Locate and identify every blood parasite.
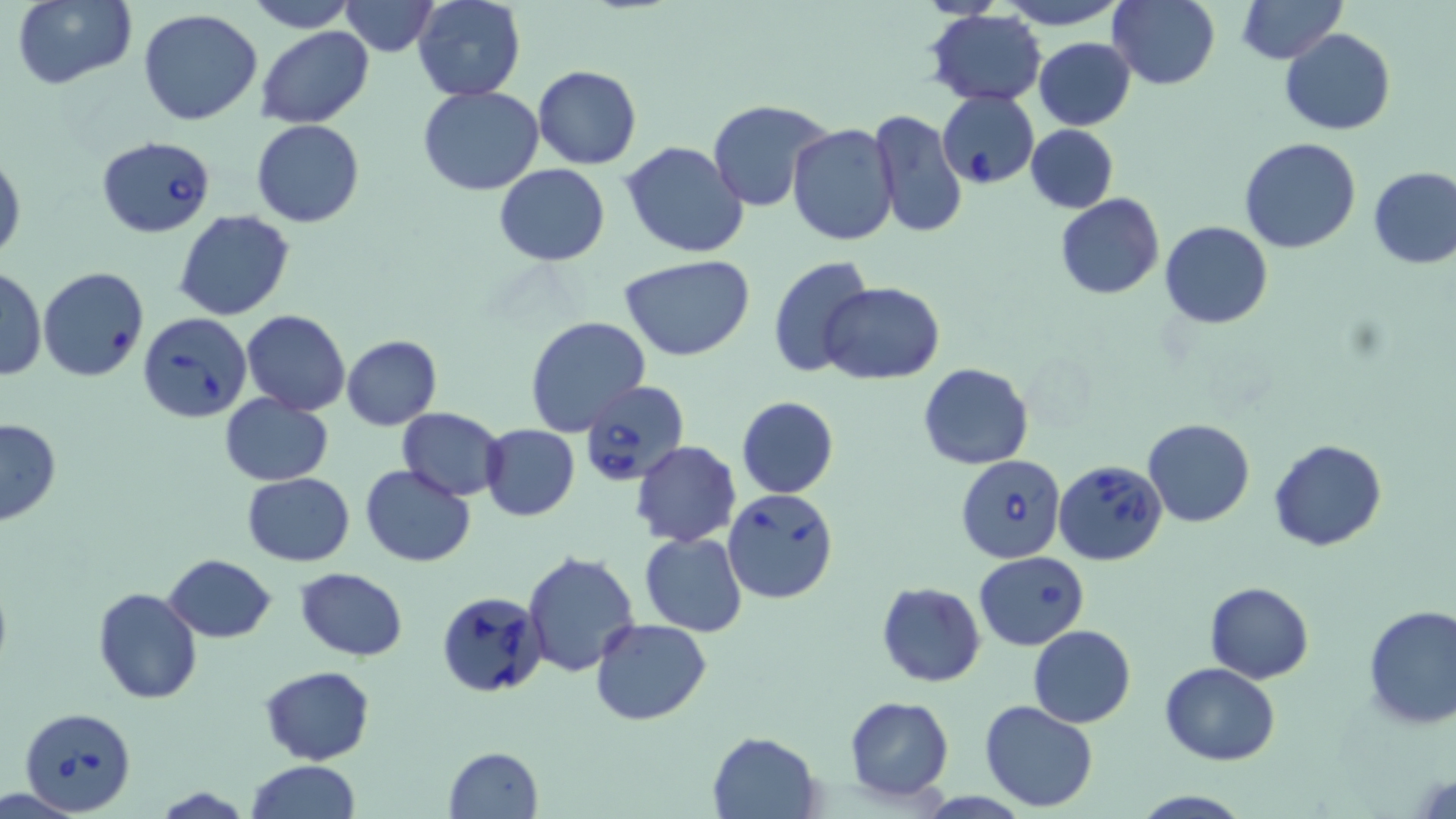
Approximate bounding boxes as (x1,y1)-(x2,y2) corner pairs in pixels.
Babesia divergens-infected red blood cells: (937,90)-(1039,189), (97,135)-(217,237), (136,311)-(252,422), (579,382)-(690,485), (955,454)-(1065,563), (1054,459)-(1168,566), (722,487)-(841,605), (436,590)-(548,699), (19,706)-(137,814).
No Plasmodium falciparum, Plasmodium ovale, Plasmodium malariae, Plasmodium vivax, or Trypanosoma brucei observed.

slide-level diagnosis = Babesia divergens
stain = May-Grünwald-Giemsa
image size = 1456×819 pixels
preparation = thin blood smear
uninfected red blood cell locations = approximate bounding boxes as (x1,y1)-(x2,y2) corner pairs in pixels: (9,0)-(141,91), (242,0)-(357,32), (412,0)-(526,102), (997,0)-(1129,29), (1108,0)-(1219,89), (1236,0)-(1344,64), (337,2)-(437,55), (924,8)-(1050,108), (138,9)-(265,127), (256,27)-(373,127), (1281,28)-(1396,135), (1033,37)-(1136,130), (533,65)-(641,168), (419,87)-(545,196), (708,99)-(837,213), (867,109)-(967,244), (251,119)-(365,229), (787,124)-(900,246), (1026,125)-(1119,212), (1241,139)-(1362,255), (620,140)-(748,258), (0,149)-(24,264), (495,164)-(609,266), (1369,166)-(1456,269), (1055,193)-(1165,300), (175,210)-(295,320), (1160,220)-(1273,329), (620,254)-(755,361), (767,255)-(877,381), (0,267)-(46,381), (38,267)-(150,382), (820,282)-(945,383), (242,309)-(351,415), (523,315)-(651,435), (340,334)-(442,431), (917,363)-(1034,470), (219,392)-(334,486), (736,396)-(839,498), (396,407)-(508,500), (0,417)-(60,525), (1142,419)-(1254,527), (480,424)-(580,521), (1268,439)-(1388,551), (631,441)-(741,547), (359,463)-(478,566), (242,471)-(355,566), (640,532)-(747,637), (521,549)-(642,679), (974,551)-(1090,650), (164,554)-(276,642), (295,566)-(407,662), (877,581)-(985,687), (1204,582)-(1313,683), (92,586)-(203,705), (1361,605)-(1456,730), (590,618)-(711,725), (1027,626)-(1136,728), (1160,662)-(1282,765), (260,666)-(375,765), (843,695)-(954,801), (979,700)-(1099,814), (709,730)-(821,818), (442,746)-(544,819), (246,759)-(361,819), (153,787)-(257,819), (1131,791)-(1253,819)
magnification = 1000x
field of view = one of a larger specimen
modality = optical microscopy